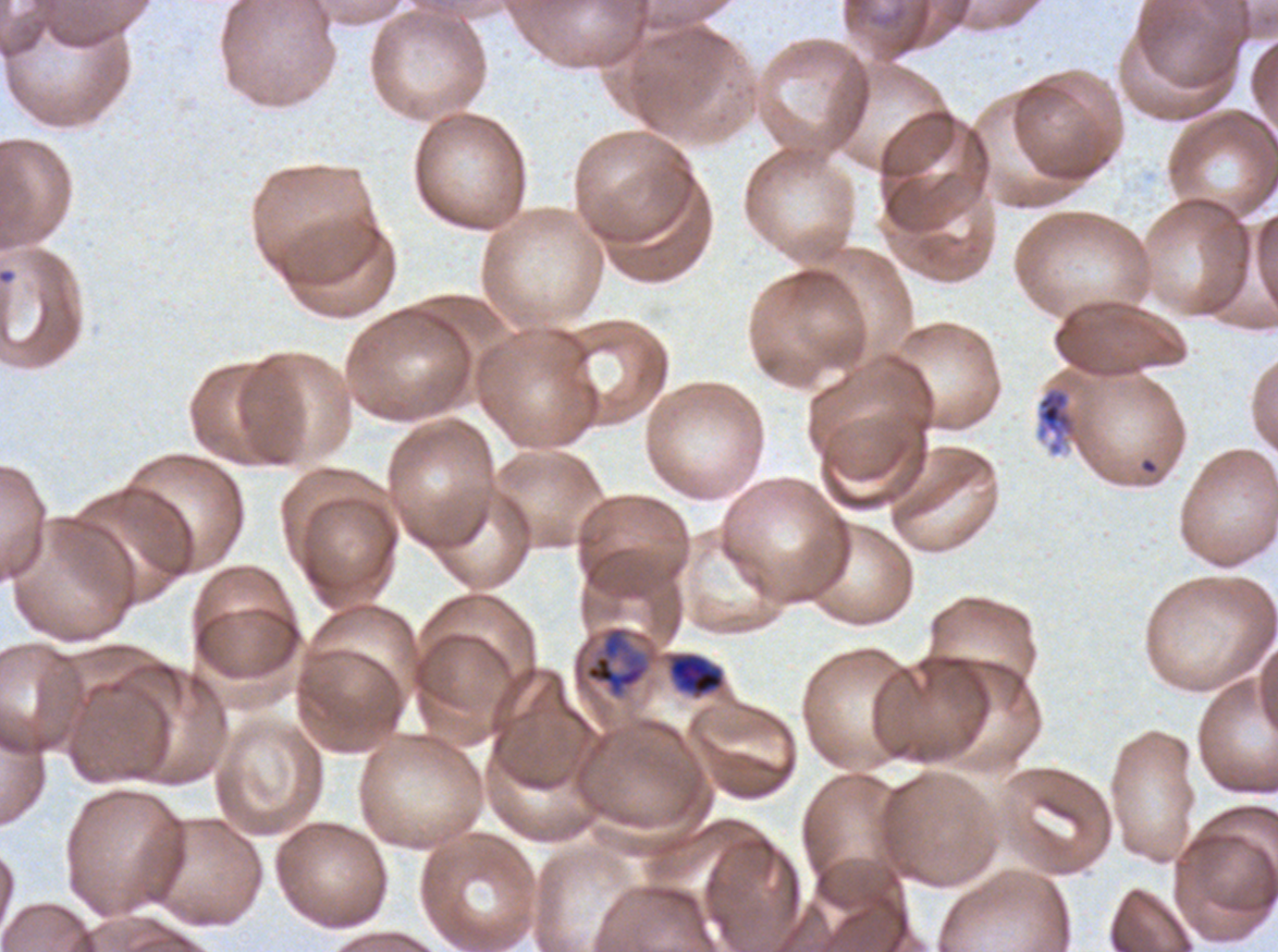 Approximate bounding boxes as (x1, y1, x2, y2) in pixels. Early schizont locations: (584, 626, 649, 698). Debris locations: (1036, 385, 1078, 456). Mid trophozoite locations: (669, 653, 724, 696). Thin blood smear. Ex-vivo Plasmodium falciparum culture from a patient in The Gambia, grown for 24 to 48 hours. Life-cycle stages observed: mid trophozoite, early schizont. A sub-image separated from a larger composite. Image is 1278×952 pixels. Giemsa stain.